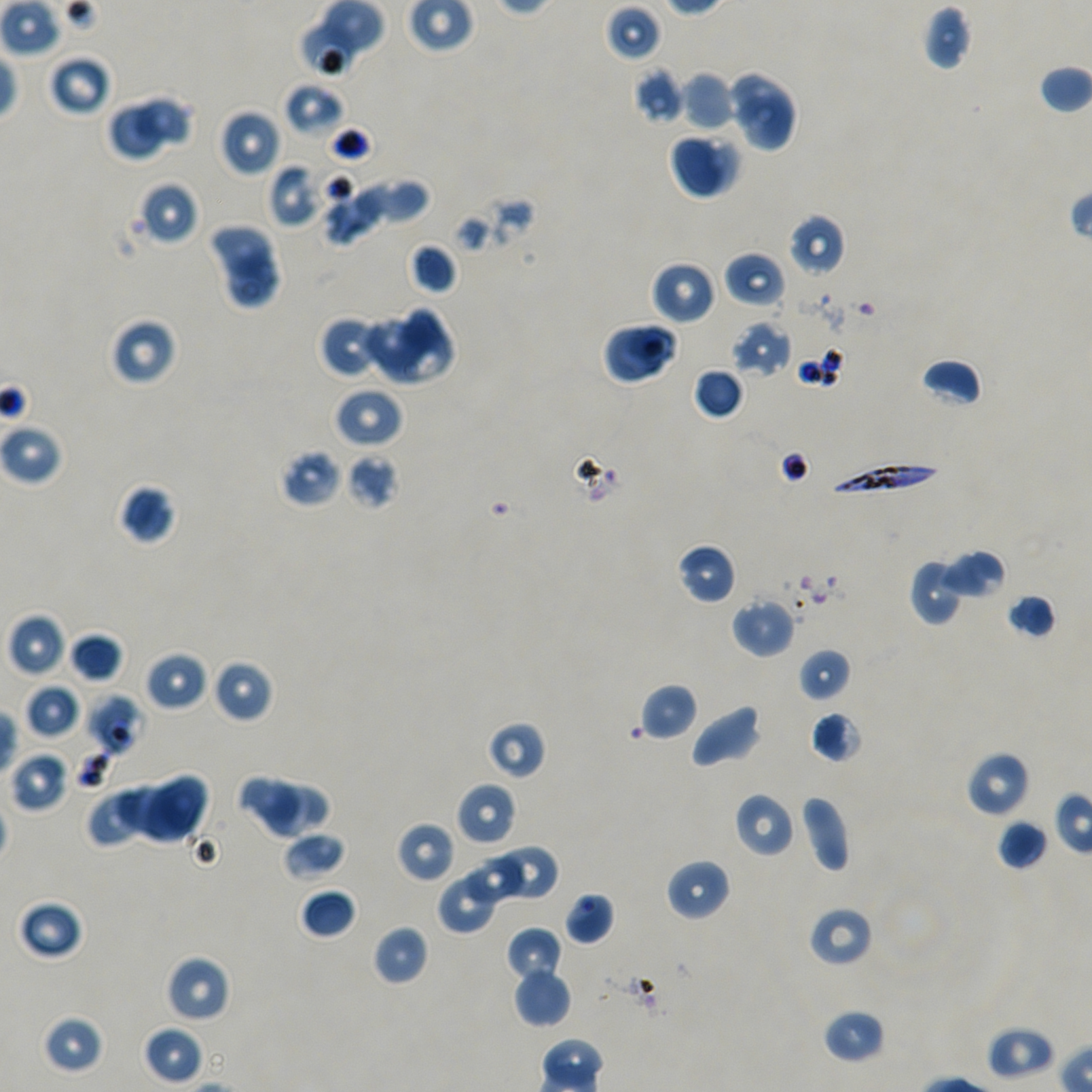
Not every red blood cell is marked.
donor blood group = A+/O+
culture = static in-vitro Plasmodium falciparum strain NF54
image size = 1092×1092 pixels
objective = 100x, oil immersion, numerical aperture 1.45
locations of infected red blood cells = approximate bounding boxes as {x1, y1, x2, y2} in pixels: {828, 460, 943, 497}
locations of red blood cells of indeterminate infection status = approximate bounding boxes as {x1, y1, x2, y2} in pixels: {299, 23, 359, 76}, {87, 692, 149, 755}, {807, 905, 873, 968}
field of view = single
locations of uninfected red blood cells = approximate bounding boxes as {x1, y1, x2, y2} in pixels: {604, 3, 662, 62}, {922, 4, 973, 71}, {48, 53, 113, 116}, {1038, 64, 1092, 115}, {634, 67, 685, 124}, {726, 69, 797, 131}, {680, 70, 736, 132}, {284, 82, 344, 136}, {731, 91, 797, 151}, {130, 94, 198, 154}, {107, 103, 168, 160}, {219, 109, 281, 177}, {668, 130, 742, 199}, {268, 163, 324, 230}, {316, 172, 400, 251}, {378, 179, 431, 227}, {139, 181, 199, 245}, {788, 213, 846, 277}, {206, 223, 281, 278}, {407, 242, 458, 295}, {723, 251, 786, 309}, {219, 252, 283, 314}, {651, 260, 718, 325}, {385, 310, 455, 385}, {109, 316, 178, 386}, {318, 316, 378, 378}, {365, 316, 425, 377}, {602, 320, 679, 385}, {731, 321, 792, 378}, {920, 358, 983, 407}, {693, 367, 745, 420}, {333, 387, 403, 448}, {0, 421, 64, 486}, {280, 448, 342, 507}, {345, 454, 399, 511}, {119, 484, 175, 544}, {676, 542, 738, 605}, {935, 549, 1006, 602}, {908, 557, 966, 625}, {1006, 593, 1057, 639}, {731, 597, 795, 659}, {7, 613, 67, 678}, {68, 633, 123, 684}, {797, 647, 853, 703}, {145, 651, 206, 711}, {211, 658, 274, 724}, {638, 682, 699, 741}, {24, 683, 81, 739}, {691, 704, 762, 768}, {810, 710, 864, 763}, {486, 720, 547, 780}, {966, 751, 1030, 818}, {10, 752, 69, 812}, {141, 774, 212, 841}, {237, 774, 304, 841}, {115, 782, 189, 845}, {263, 782, 333, 836}, {456, 782, 517, 847}, {86, 788, 142, 849}, {733, 791, 795, 858}, {799, 795, 850, 873}, {996, 818, 1049, 871}, {396, 822, 456, 883}, {283, 831, 348, 881}, {496, 843, 560, 903}, {466, 853, 524, 907}, {666, 858, 731, 922}, {437, 865, 507, 935}, {299, 888, 357, 940}, {564, 892, 615, 946}, {17, 898, 85, 960}, {372, 924, 429, 986}, {505, 927, 563, 984}, {165, 955, 231, 1023}, {512, 966, 572, 1027}, {822, 1008, 886, 1064}, {41, 1013, 105, 1074}, {142, 1025, 204, 1085}, {987, 1026, 1056, 1079}
preparation = thin blood smear
stain = Giemsa